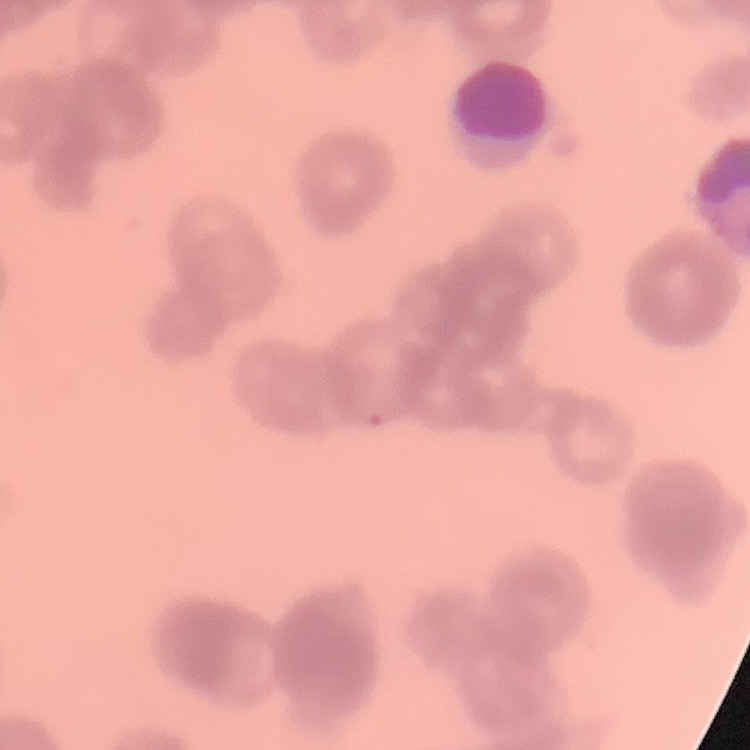 The red blood cells exhibit rouleaux formation. Thin blood film. Stained with either Field's or Giemsa. One tile cut from a larger photomicrograph.